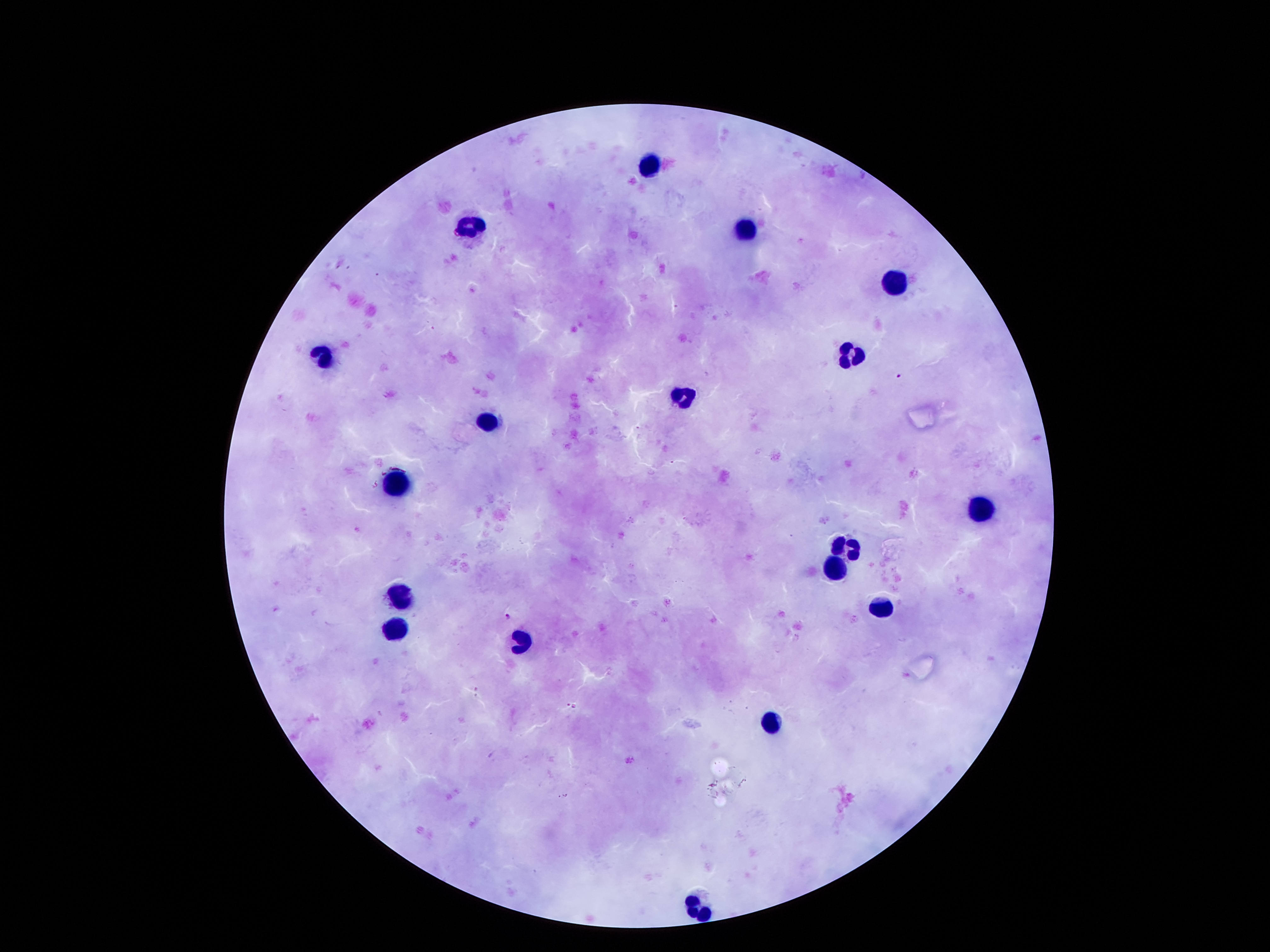

coordinate format = approximate centers as [x, y] in pixels
malaria parasite locations = [899, 375], [509, 616], [570, 704]
leukocyte locations = [648, 166], [473, 227], [744, 233], [892, 281], [322, 354], [852, 355], [683, 399], [489, 422], [398, 483], [979, 506], [846, 549], [837, 572], [400, 598], [882, 606], [393, 633], [523, 643], [770, 722], [696, 908]
stain = Giemsa
magnification = 100x
capture = smartphone camera through the microscope eyepiece
patient malaria status = positive for Plasmodium falciparum
field of view = one from this slide
preparation = thick blood film
image size = 1270×952 pixels